State which parasite is depicted.
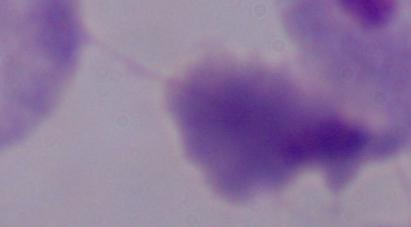

This is a trichomonad.

modality = micrograph
magnification = 1000x